Identify the parasite.
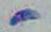

This is Toxoplasma gondii.

Summary:
  - Modality: photomicrograph
  - Magnification: 1000x